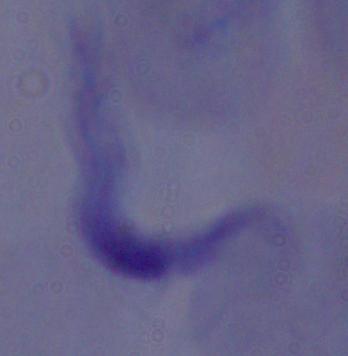
1000x magnification. Photomicrograph. A trypanosome is seen.